Describe the morphology of the erythrocytes.
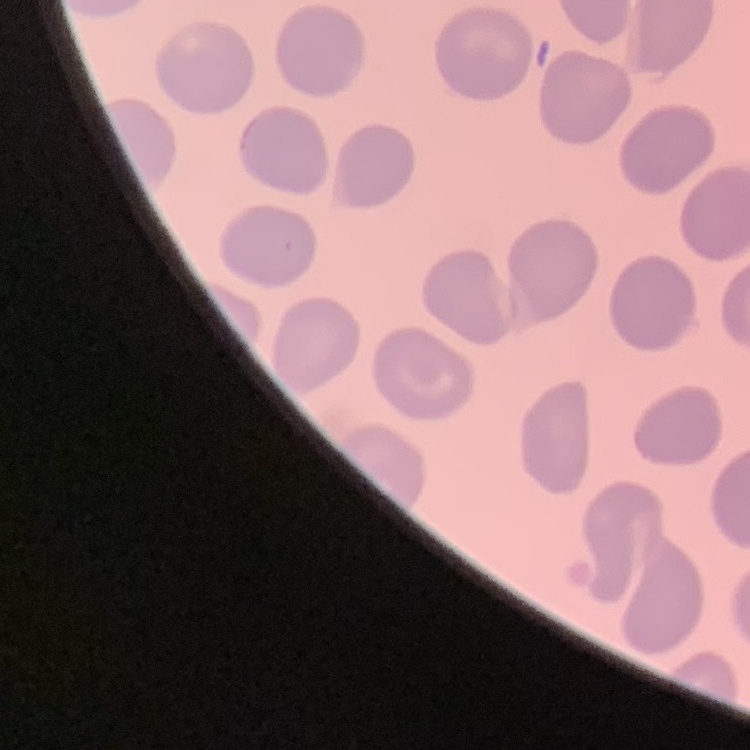

They show no rouleaux formation.

Square crop of a larger photomicrograph. Thin blood film. Field's or Giemsa stain.